Identify the parasite.
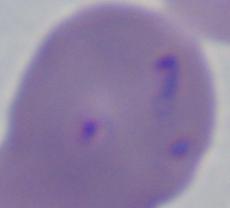
This is Babesia.

Photomicrograph. 1000x magnification.